Report the malaria status of this cell.
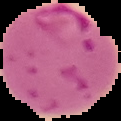

Parasitized.

Summary:
  - Image size: 121×121 pixels
  - Preparation: thin blood film
  - Image type: cell region segmented out of the field of view; surrounding area masked to black